Classify this cell by malaria status.
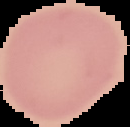
It is uninfected.

Image is 130×127 pixels. From a thin blood smear. Cell region segmented out of the field of view; the surrounding area is masked to black.